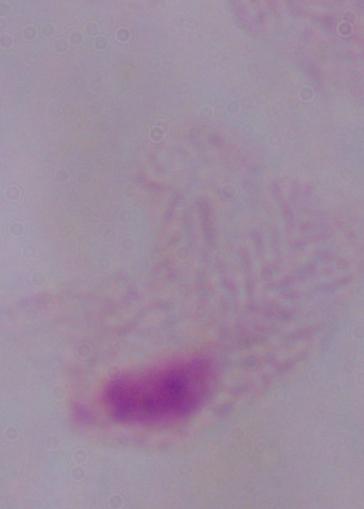

Summary:
  - Identification: trichomonad
  - Modality: photomicrograph
  - Magnification: 1000x